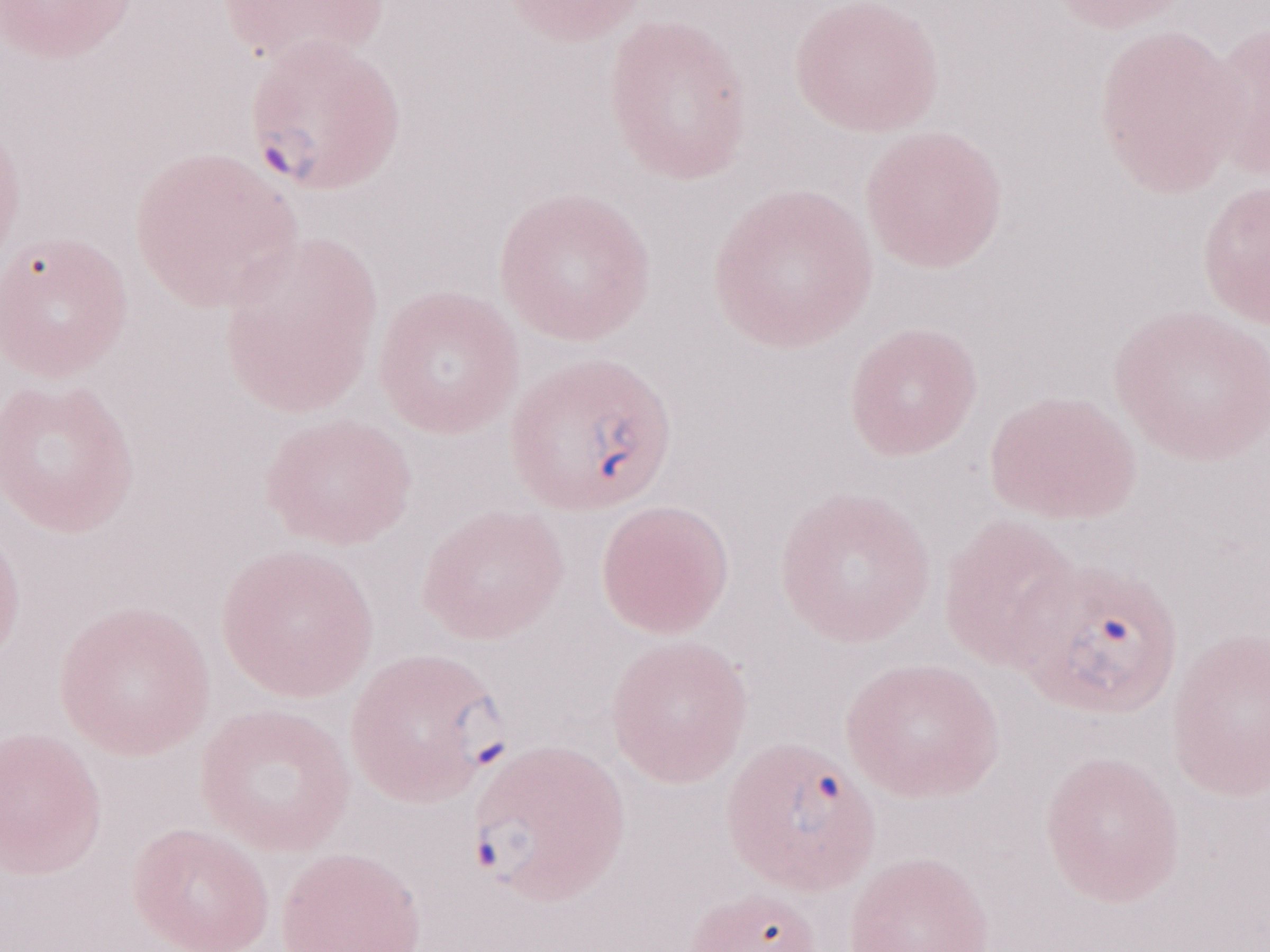
Olympus BX43 microscope and DP73 digital camera. Single field of view. Image is 1270×952 pixels. 1,000x magnification. May-Grünwald-Giemsa stain. Thin blood smear. Patient-level malaria diagnosis: positive.